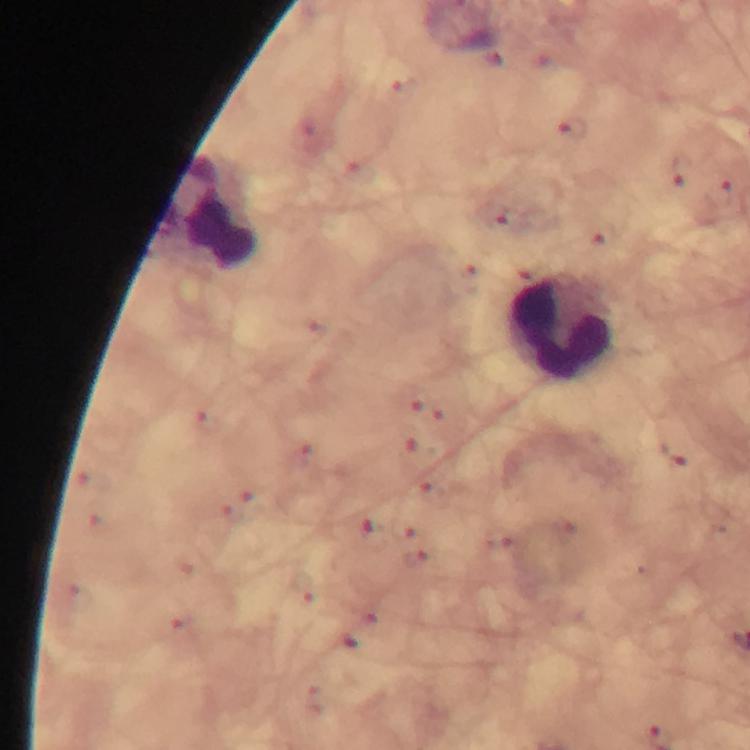

capture = smartphone camera through the microscope
stain = Giemsa
cropped from = a single field of view
preparation = thick blood smear
magnification = 100x
leukocyte locations = approximate object centers, in pixels from the top-left corner: (x=210, y=213), (x=564, y=327)
immersion oil = applied
malaria parasite locations = approximate object centers, in pixels from the top-left corner: (x=571, y=130), (x=682, y=169), (x=720, y=192), (x=509, y=218), (x=678, y=453)
image size = 750×750 pixels
context = from a diagnostic examination for malaria